Find the cells and give the type of each one.
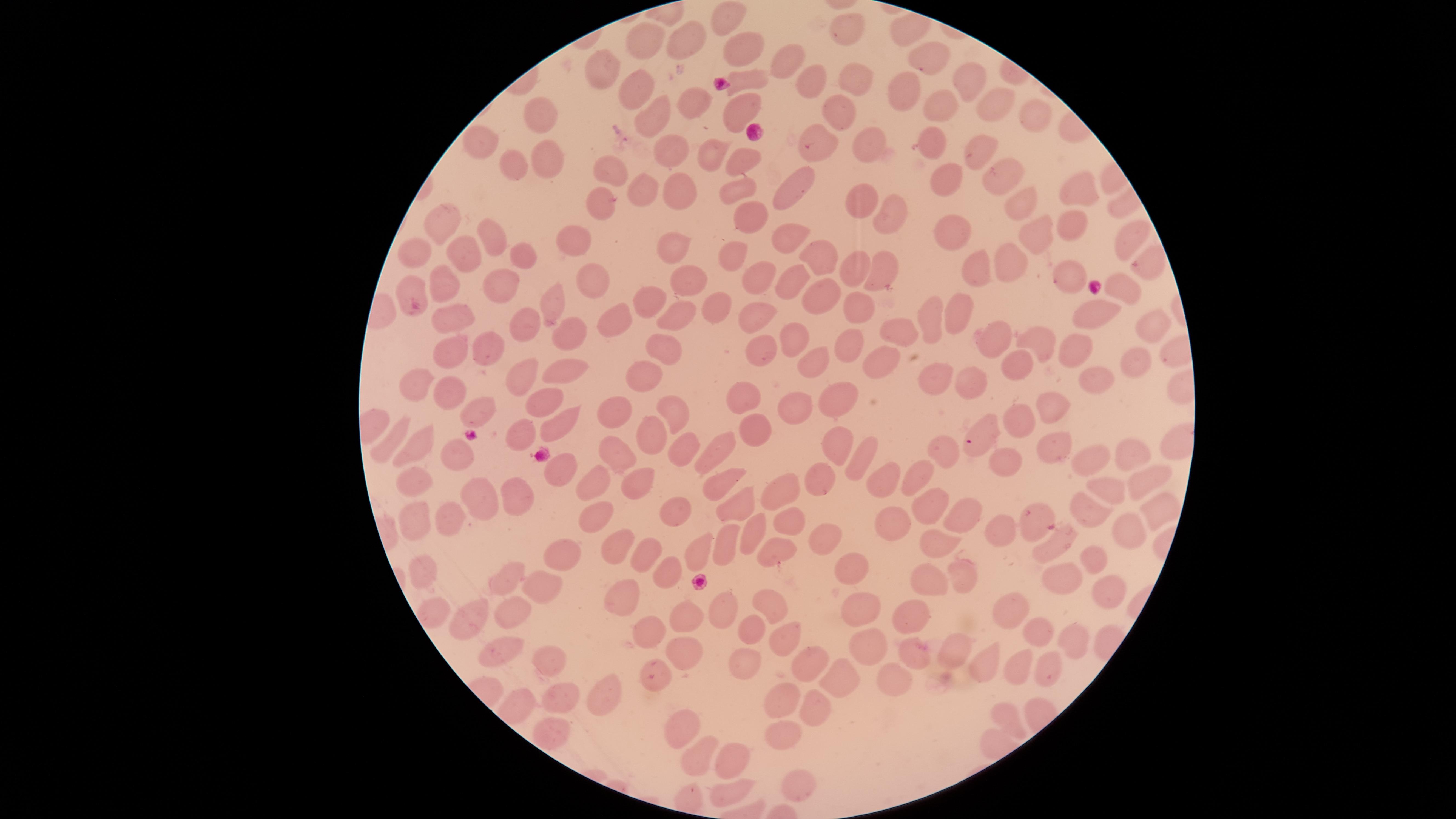
No parasitized RBCs identified.
Approximate marker points as (x, y) in pixels.
Uninfected RBCs: (732, 17), (852, 34), (679, 35), (644, 40), (751, 48), (796, 57), (932, 58), (606, 69), (810, 77), (748, 79), (972, 83), (851, 84), (634, 89), (901, 90), (993, 106), (683, 108), (937, 108), (838, 110), (741, 111), (653, 113), (545, 115), (1030, 115), (486, 138), (813, 138), (928, 139), (663, 150), (867, 151), (715, 154), (546, 158), (513, 161), (972, 161), (615, 166), (747, 166), (943, 177), (645, 184), (734, 184), (791, 184), (1004, 184), (678, 186), (1076, 194), (604, 197), (859, 198), (1027, 210), (889, 213), (749, 216), (447, 220), (959, 227), (1071, 227), (488, 235), (791, 235), (1035, 237), (584, 238), (675, 244), (1128, 244), (420, 246), (519, 252), (732, 253), (820, 253), (457, 260), (1006, 263), (981, 266), (854, 272), (877, 273), (693, 276), (759, 276), (1067, 277), (592, 278), (789, 280), (504, 282), (444, 285), (417, 287), (1123, 289), (654, 298), (813, 299), (859, 305), (553, 306), (717, 307), (1099, 311), (958, 312), (679, 314), (615, 317), (456, 318), (761, 319), (938, 319), (903, 322), (529, 327), (570, 331), (1152, 331), (792, 338), (996, 340), (1044, 343), (851, 346), (1074, 346), (661, 347), (484, 350), (756, 351), (445, 355), (883, 358), (816, 360), (1136, 362), (1015, 363), (563, 367), (525, 370), (640, 372), (934, 375), (972, 376), (1094, 380), (418, 382), (454, 389), (547, 395), (828, 396), (748, 397), (795, 403), (675, 409), (612, 410), (1046, 410), (481, 413), (1018, 419), (558, 421), (983, 429), (756, 430), (650, 432), (521, 433), (386, 442), (721, 443), (831, 443), (685, 448), (1053, 448), (1137, 449), (456, 456), (617, 456), (865, 456), (941, 456), (416, 457), (1101, 457), (1008, 458), (558, 467), (922, 473), (893, 475), (637, 476), (1142, 476), (721, 479), (819, 479), (592, 483), (414, 485), (778, 485), (1112, 485), (514, 491), (476, 498), (743, 499), (671, 500), (930, 505), (1090, 508), (891, 509), (1152, 511), (1034, 514), (414, 516), (789, 516), (448, 519), (962, 520), (591, 524), (758, 524), (1003, 531), (822, 535), (1121, 535), (730, 541), (1056, 544), (696, 546), (621, 549), (939, 549), (642, 554), (782, 554), (560, 556), (1093, 558), (420, 567), (851, 567), (668, 571), (1058, 573), (960, 574), (932, 578), (504, 579), (543, 583), (1108, 585), (627, 593), (856, 598), (725, 604), (768, 604), (1018, 604), (514, 612), (917, 612), (436, 615), (691, 618), (471, 622), (749, 628), (649, 632), (1042, 632), (786, 633), (1078, 643), (496, 647), (682, 648), (952, 648), (916, 649), (865, 652), (1018, 656), (744, 657), (1050, 657), (811, 662), (990, 663), (543, 665), (655, 668), (893, 677), (835, 683), (606, 696), (558, 697), (774, 702), (813, 706), (1005, 710), (677, 716), (554, 731), (780, 733), (695, 747), (727, 760), (793, 789), (721, 792).
No WBCs identified.

Summary:
  - Capture: smartphone photograph through the microscope eyepiece
  - Preparation: thin blood film
  - Image size: 1456×819 pixels
  - Stain: Giemsa
  - Visible region: circular
  - Field of view: single